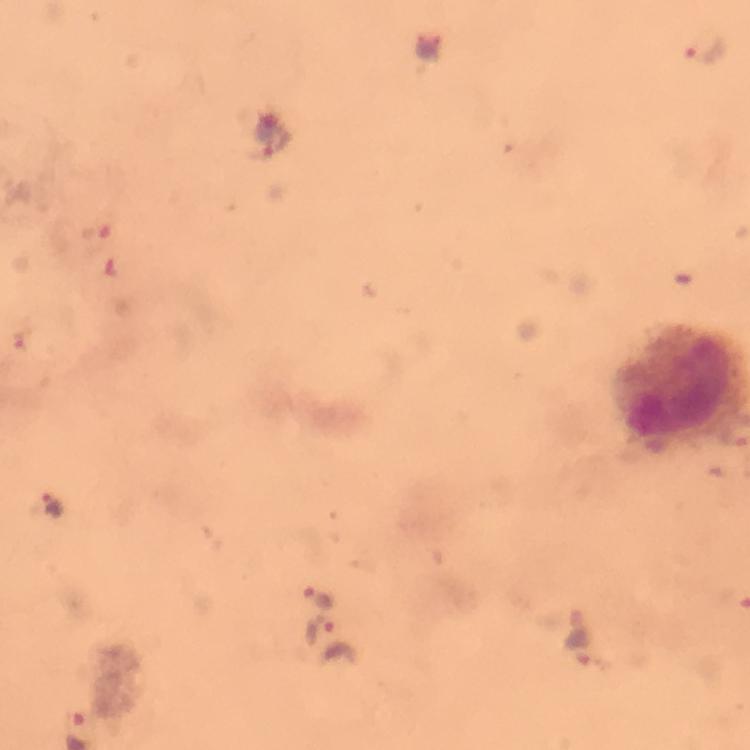
Approximate object centers, in pixels from the top-left corner.
Summary:
  - Malaria parasite locations: (x=706, y=47), (x=278, y=142), (x=51, y=505), (x=315, y=595), (x=318, y=627)
  - Stain: Giemsa
  - Cropped from: a single field of view
  - Immersion oil: applied
  - Context: from a diagnostic examination for malaria
  - Capture: smartphone camera through the microscope
  - Preparation: thick smear
  - Image size: 750×750 pixels
  - Magnification: 100x